Classify this cell by malaria status.
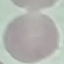

Uninfected.

Summary:
  - Capture: smartphone through the microscope eyepiece
  - Preparation: thin blood film
  - Stain: Giemsa
  - Image type: automatically extracted cell patch, resized to 64 × 64 pixels